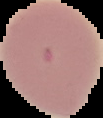
From a thin blood smear. Result: negative for Plasmodium parasites. Image is 103×118 pixels. Cell region segmented out of the field of view; the surrounding area is masked to black.